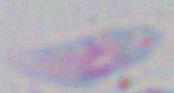 Toxoplasma gondii is shown. Photomicrograph. 1000x magnification.